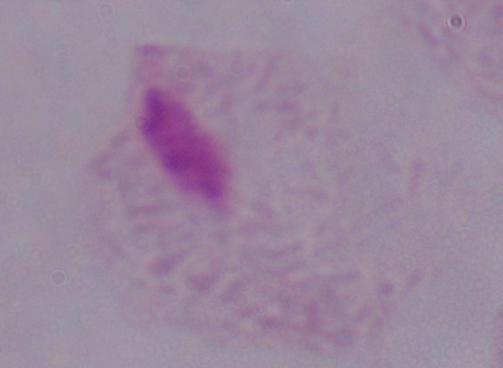
1000x magnification. Micrograph. A trichomonad is shown.